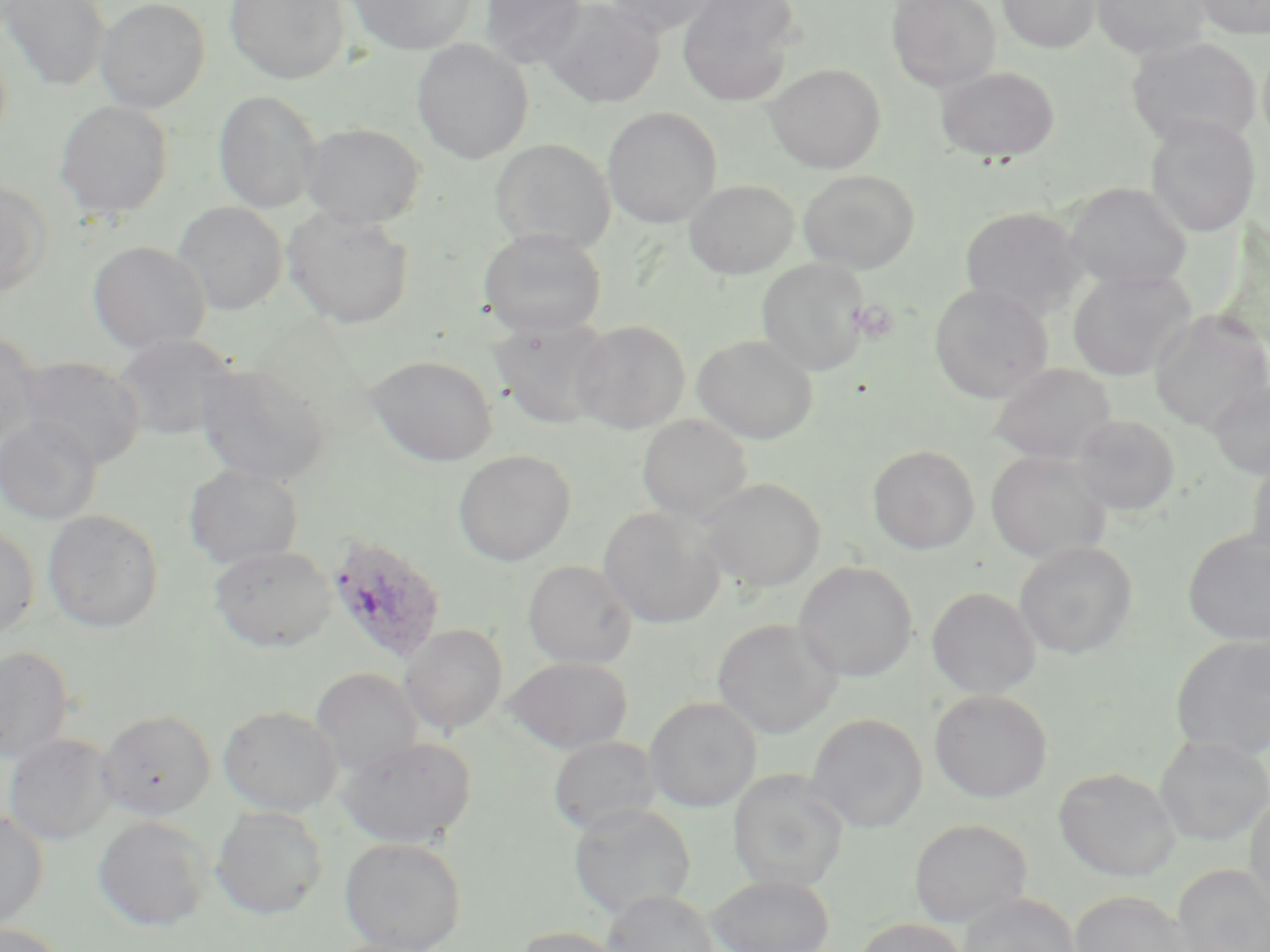
{
  "slide_level_diagnosis": "Plasmodium ovale",
  "uninfected_red_blood_cell_locations": "approximate bounding boxes as [x1, y1, x2, y2] in pixels: [95, 0, 210, 113], [224, 0, 350, 84], [346, 0, 477, 55], [478, 0, 585, 69], [539, 0, 664, 108], [603, 0, 720, 36], [676, 0, 802, 106], [886, 0, 1001, 91], [997, 0, 1100, 53], [1091, 0, 1211, 60], [1189, 0, 1270, 39], [2, 1, 109, 91], [1126, 37, 1261, 149], [412, 38, 534, 164], [1258, 42, 1270, 153], [765, 63, 885, 173], [935, 66, 1060, 163], [213, 90, 323, 214], [54, 101, 173, 220], [602, 106, 722, 228], [1145, 114, 1260, 237], [301, 122, 426, 230], [489, 138, 615, 253], [798, 169, 920, 274], [683, 179, 799, 279], [0, 182, 51, 300], [1064, 182, 1192, 292], [173, 201, 289, 314], [959, 206, 1089, 320], [283, 207, 414, 329], [478, 228, 607, 339], [88, 240, 211, 353], [756, 257, 871, 376], [1068, 269, 1196, 382], [929, 283, 1054, 403], [1149, 310, 1270, 432], [489, 317, 614, 430], [572, 320, 690, 434], [0, 329, 39, 450], [113, 333, 239, 440], [693, 335, 817, 444], [366, 355, 497, 465], [14, 356, 146, 468], [195, 361, 333, 485], [988, 363, 1118, 465], [1208, 379, 1269, 480], [637, 414, 752, 523], [1072, 414, 1180, 516], [0, 417, 102, 525], [867, 445, 980, 554], [454, 450, 576, 565], [985, 450, 1112, 565], [1246, 454, 1270, 570], [184, 462, 304, 570], [697, 477, 825, 592], [598, 507, 725, 629], [43, 509, 164, 632], [0, 525, 40, 639], [1182, 530, 1270, 645], [1014, 541, 1137, 660], [209, 545, 337, 651], [523, 560, 637, 668], [793, 561, 918, 683], [926, 586, 1042, 699], [712, 618, 842, 739], [400, 624, 508, 734], [1170, 634, 1269, 760], [0, 645, 74, 763], [503, 656, 633, 753], [311, 667, 423, 776], [929, 689, 1052, 803], [644, 696, 761, 812], [219, 705, 342, 816], [99, 710, 216, 820], [806, 713, 927, 833], [4, 733, 118, 845], [1155, 735, 1270, 846], [337, 736, 476, 848], [548, 736, 660, 835], [1053, 767, 1181, 881], [728, 770, 849, 892], [1245, 794, 1270, 917], [567, 803, 697, 920], [211, 806, 328, 920], [0, 810, 49, 930], [93, 816, 212, 932], [910, 819, 1032, 928], [339, 836, 467, 952], [1172, 864, 1269, 952], [706, 874, 835, 951], [602, 890, 719, 952], [1069, 890, 1191, 952], [957, 893, 1082, 952], [855, 918, 969, 952], [0, 922, 68, 952], [513, 926, 628, 952]",
  "field_of_view": "single",
  "stain": "May-Grünwald-Giemsa",
  "platelet_locations": "approximate bounding boxes as [x1, y1, x2, y2] in pixels: [849, 298, 900, 344]",
  "plasmodium_ovale_infected_red_blood_cell_locations": "approximate bounding boxes as [x1, y1, x2, y2] in pixels: [324, 531, 447, 666]",
  "modality": "optical microscopy",
  "magnification": "1000x",
  "image_size": "1270×952 pixels",
  "preparation": "thin blood smear"
}